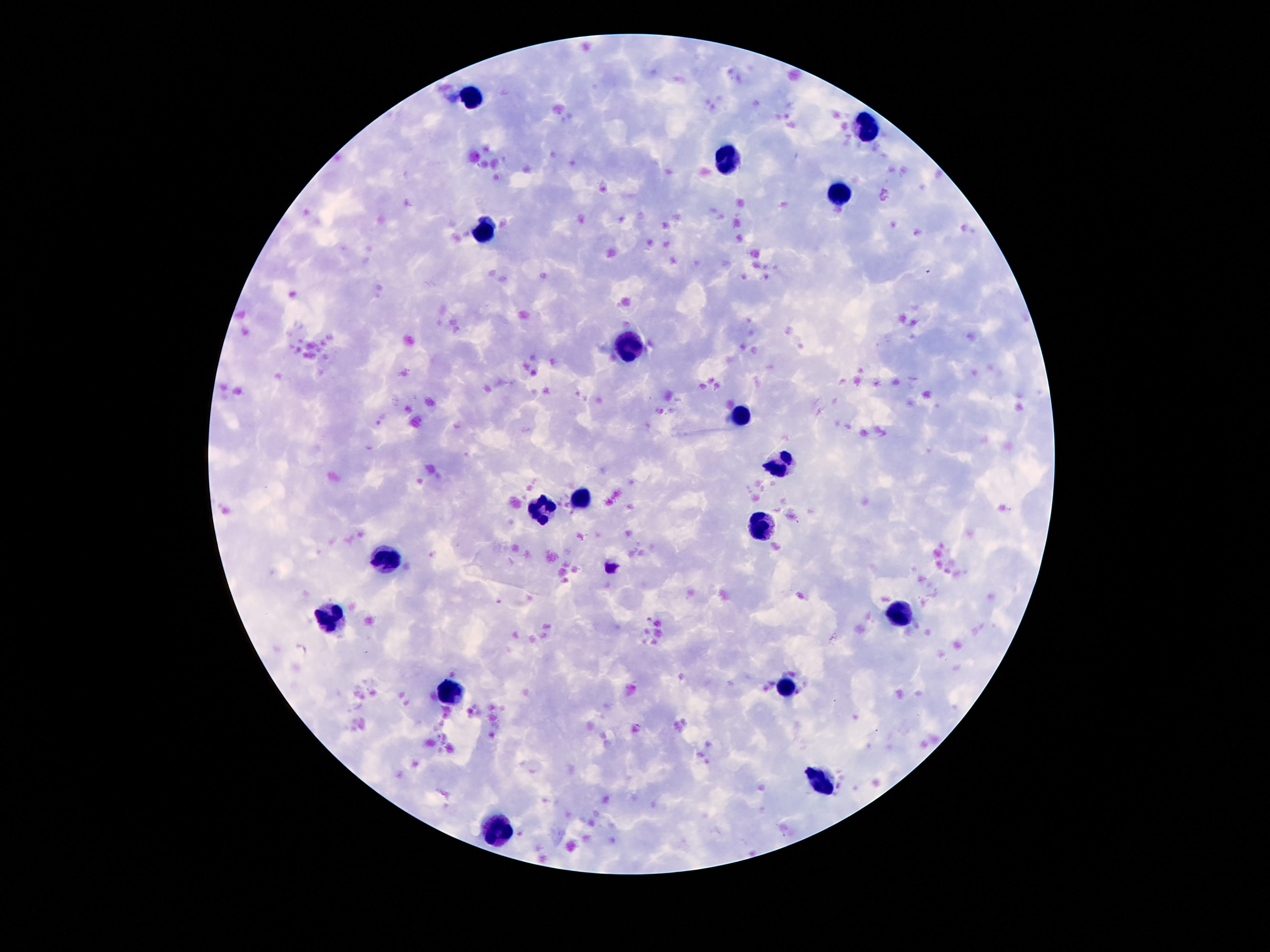

patient malaria status = negative
magnification = 100x
capture = smartphone camera through the microscope eyepiece
stain = Giemsa
field of view = one from this slide
leukocyte locations = approximate centers as (x, y) in pixels: (471, 98), (866, 124), (725, 163), (837, 190), (487, 227), (624, 341), (739, 417), (784, 464), (581, 497), (540, 509), (762, 530), (385, 560), (895, 612), (331, 616), (782, 688), (450, 696), (823, 784), (497, 827)
image size = 1270×952 pixels
preparation = thick blood film